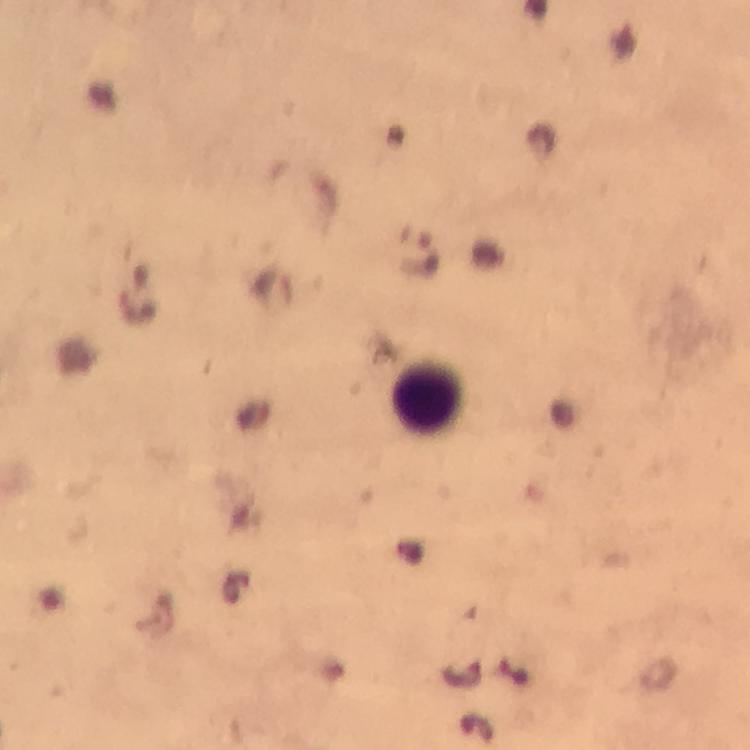

{
  "cropped_from": "a single field of view",
  "context": "from a malaria diagnostic workup",
  "magnification": "100x",
  "preparation": "thick smear",
  "stain": "Giemsa",
  "malaria_parasite_locations": "approximate centers as (x, y) in pixels: (423, 255)",
  "capture": "smartphone photograph through a microscope",
  "image_size": "750×750 pixels",
  "leukocyte_locations": "approximate centers as (x, y) in pixels: (428, 399)",
  "immersion_oil": "used"
}